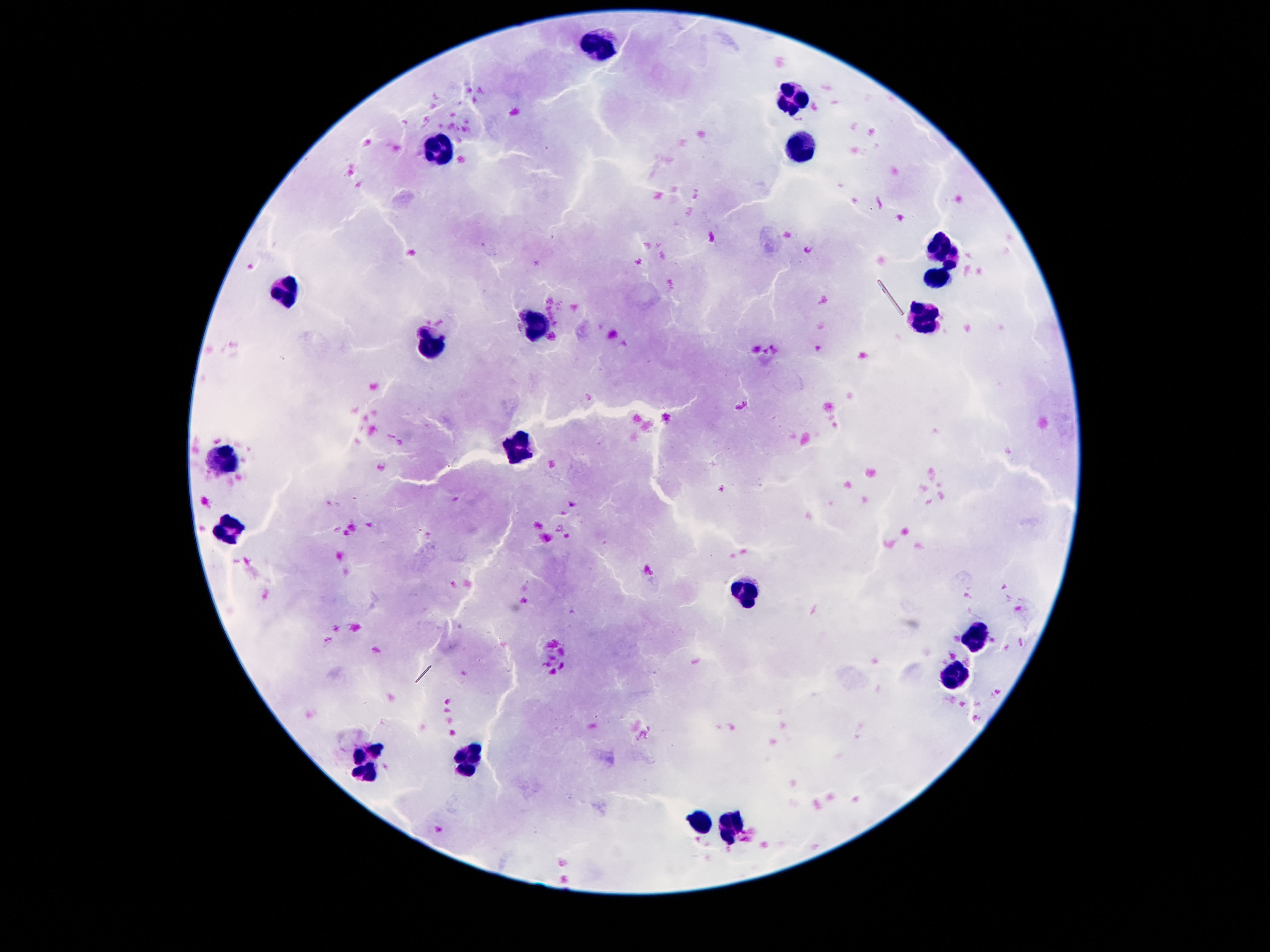
Approximate centers as (x, y) in pixels.
Summary:
  - Leukocyte locations: (597, 44), (796, 98), (441, 145), (796, 149), (945, 251), (939, 280), (286, 294), (923, 312), (536, 325), (431, 347), (525, 448), (224, 464), (230, 528), (745, 591), (976, 634), (958, 675), (468, 759), (368, 763), (699, 821), (730, 823)
  - Preparation: thick peripheral-blood smear
  - Stain: Giemsa
  - Image size: 1270×952 pixels
  - Field of view: one from this slide
  - Magnification: 100x
  - Patient malaria status: not infected
  - Capture: smartphone camera through the microscope eyepiece